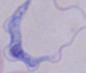
Summary:
  - Identification: trypanosome
  - Magnification: 1000x
  - Modality: micrograph